Assess the morphology of the erythrocytes.
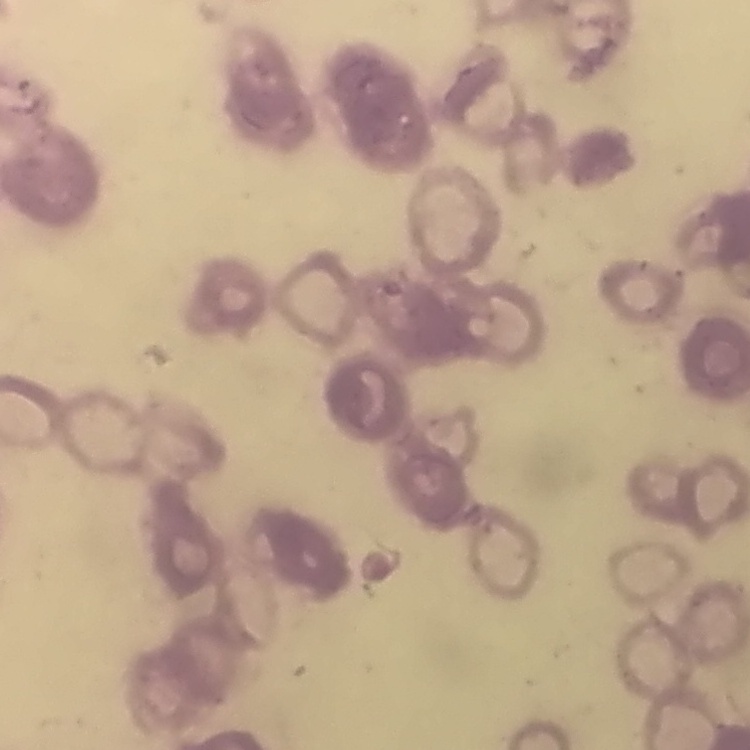

Rouleaux formation.

stain: Field's or Giemsa
preparation: thin blood film
image_type: one tile cut from a larger photomicrograph